Point out each Plasmodium parasite.
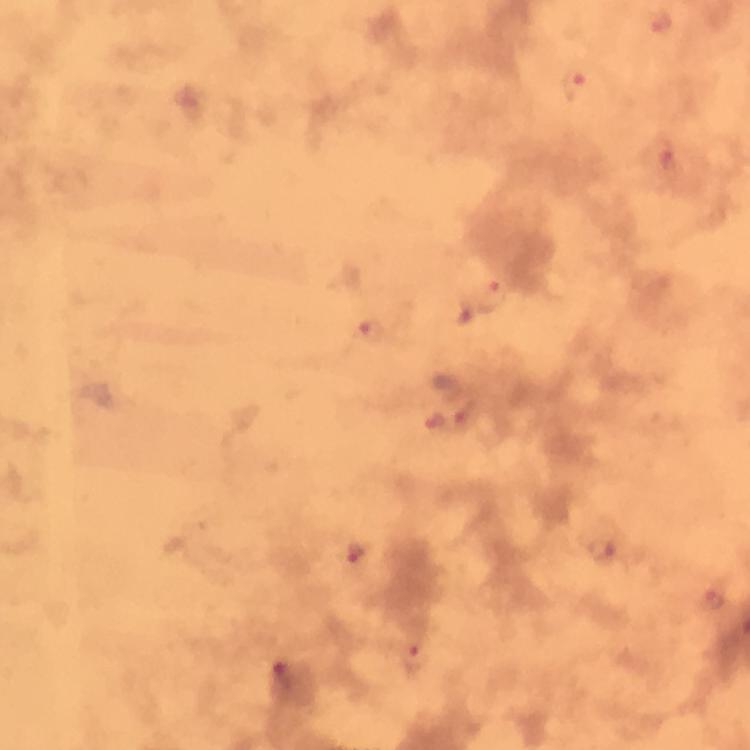
Approximate centers as [x, y] in pixels.
Plasmodium parasites: [658, 22], [575, 86], [666, 159], [494, 291], [370, 328], [466, 414], [432, 423], [358, 552], [601, 552], [713, 599], [416, 657], [283, 672].

Summary:
  - Stain: Giemsa
  - Cropped from: one field of view
  - Magnification: 100x
  - Context: from a diagnostic examination for malaria
  - Preparation: thick blood smear
  - Capture: smartphone mounted on the microscope
  - Immersion oil: used
  - Image size: 750×750 pixels